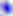
Micrograph. Toxoplasma gondii is seen. 400x magnification.